Report the malaria status of this cell.
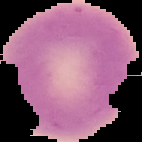
It is uninfected.

Summary:
  - Image type: segmented cell region with the area outside set to black
  - Image size: 142×142 pixels
  - Preparation: thin blood smear